Assess this cell for malaria.
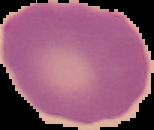

It is uninfected.

From a thin blood smear. Cell region segmented out of the field of view; the surrounding area is masked to black. Image is 154×130 pixels.